Locate every cell, classifying each as a parasitized RBC, an uninfected RBC, or a WBC.
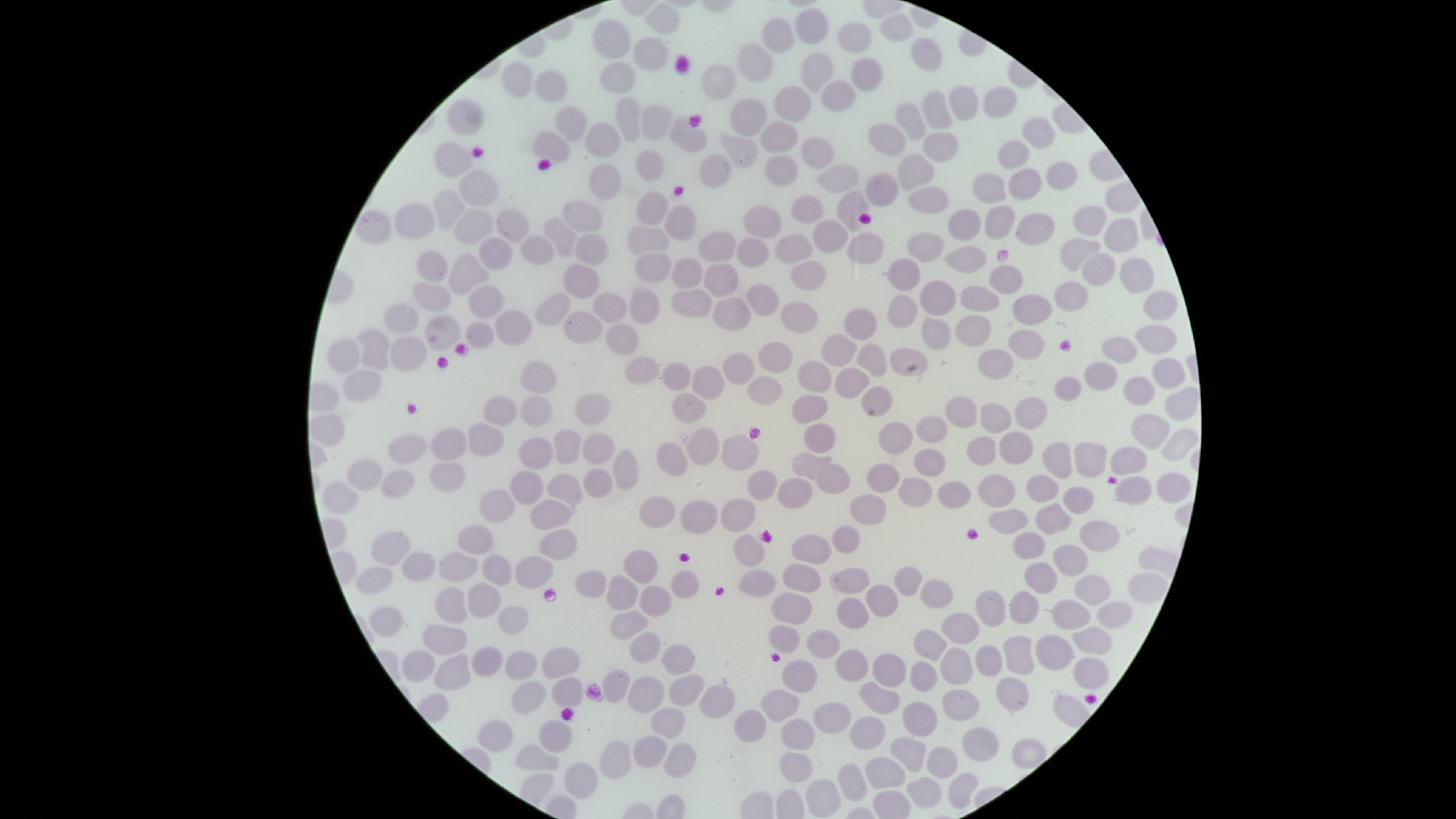
No parasitized RBCs identified.
Approximate bounding boxes as [left, top, right, bottom] in pixels.
Uninfected RBCs: [646, 4, 679, 34], [796, 9, 827, 43], [880, 15, 912, 41], [762, 17, 794, 53], [592, 20, 630, 60], [838, 24, 870, 53], [633, 37, 667, 72], [912, 37, 942, 71], [738, 43, 773, 81], [802, 52, 832, 90], [851, 58, 884, 92], [502, 62, 532, 98], [600, 62, 635, 93], [702, 64, 737, 100], [535, 72, 567, 101], [823, 82, 855, 114], [948, 84, 978, 121], [983, 85, 1017, 118], [774, 87, 810, 121], [922, 90, 953, 130], [616, 97, 639, 142], [729, 98, 766, 137], [449, 101, 483, 136], [895, 102, 925, 140], [643, 104, 671, 141], [556, 107, 588, 141], [1022, 117, 1055, 149], [670, 118, 707, 151], [586, 122, 621, 157], [761, 123, 798, 153], [869, 124, 906, 156], [534, 131, 569, 162], [719, 133, 758, 169], [924, 133, 957, 162], [801, 138, 834, 169], [997, 140, 1030, 169], [435, 142, 472, 177], [636, 150, 662, 181], [698, 153, 732, 188], [897, 154, 934, 189], [764, 156, 797, 185], [1046, 162, 1078, 190], [817, 163, 860, 194], [587, 164, 621, 201], [1008, 168, 1042, 200], [459, 170, 497, 206], [865, 173, 897, 206], [973, 173, 1006, 203], [909, 187, 949, 214], [837, 190, 870, 232], [433, 191, 465, 230], [637, 193, 667, 225], [792, 195, 822, 225], [563, 201, 602, 232], [395, 204, 435, 239], [665, 205, 695, 240], [742, 205, 783, 239], [984, 206, 1016, 240], [1074, 206, 1106, 235], [354, 209, 392, 243], [454, 210, 492, 243], [497, 210, 528, 242], [949, 210, 980, 241], [1016, 213, 1055, 245], [544, 216, 577, 258], [1105, 218, 1139, 252], [811, 221, 848, 253], [628, 226, 670, 254], [699, 231, 735, 264], [845, 232, 884, 264], [908, 233, 944, 262], [775, 234, 813, 265], [520, 235, 553, 265], [576, 235, 607, 266], [478, 237, 513, 270], [737, 237, 769, 268], [1060, 239, 1099, 271], [945, 246, 988, 273], [418, 250, 447, 282], [449, 252, 489, 296], [636, 253, 672, 282], [1082, 254, 1114, 286], [1120, 256, 1154, 293], [888, 258, 920, 291], [671, 259, 702, 289], [790, 260, 826, 290], [703, 263, 738, 297], [564, 264, 598, 298], [989, 264, 1023, 294], [919, 281, 955, 316], [1055, 282, 1088, 311], [412, 283, 451, 311], [747, 284, 778, 315], [469, 285, 503, 318], [960, 286, 999, 312], [671, 289, 712, 318], [630, 290, 660, 324], [1143, 290, 1178, 320], [593, 292, 627, 323], [536, 294, 570, 326], [888, 294, 917, 329], [1013, 294, 1052, 325], [714, 298, 751, 331], [781, 301, 818, 332], [383, 304, 419, 335], [843, 308, 877, 342], [496, 310, 533, 344], [564, 310, 602, 344], [426, 315, 460, 350], [956, 315, 991, 345], [920, 317, 951, 350], [466, 322, 494, 351], [607, 325, 639, 357], [1136, 326, 1176, 354], [357, 330, 389, 370], [1009, 331, 1044, 358], [821, 334, 857, 366], [391, 337, 426, 370], [1102, 338, 1136, 363], [328, 339, 360, 372], [758, 341, 793, 373], [856, 343, 887, 378], [890, 348, 928, 376], [978, 350, 1012, 378], [721, 353, 754, 385], [625, 356, 660, 385], [1153, 358, 1185, 390], [520, 360, 557, 394], [797, 361, 832, 391], [662, 363, 691, 391], [1084, 363, 1117, 391], [693, 366, 725, 400], [836, 367, 870, 398], [344, 370, 382, 402], [749, 376, 783, 404], [1122, 376, 1155, 406], [1056, 378, 1081, 402], [863, 385, 893, 416], [673, 393, 707, 423], [576, 394, 610, 426], [792, 395, 828, 423], [520, 396, 551, 426], [946, 396, 976, 428], [483, 397, 516, 426], [1015, 398, 1046, 429], [979, 403, 1011, 432], [1132, 413, 1170, 449], [917, 416, 947, 442], [879, 422, 913, 455], [468, 423, 504, 456], [804, 424, 836, 452], [688, 427, 719, 465], [1163, 427, 1198, 461], [433, 429, 467, 461], [554, 430, 581, 464], [1000, 432, 1034, 465], [583, 433, 615, 464], [723, 434, 758, 470], [389, 436, 425, 465], [967, 436, 996, 467], [519, 437, 554, 470], [1044, 441, 1072, 480], [657, 442, 689, 477], [1073, 442, 1106, 478], [613, 448, 638, 490], [914, 448, 944, 476], [1110, 448, 1146, 473], [793, 452, 831, 480], [348, 458, 384, 490], [430, 462, 466, 491], [815, 463, 850, 494], [867, 464, 899, 493], [584, 469, 613, 498], [748, 469, 775, 500], [381, 470, 416, 499], [511, 471, 544, 505], [547, 473, 583, 507], [1156, 473, 1190, 503], [978, 474, 1015, 508], [1026, 475, 1059, 502], [779, 477, 811, 509], [898, 477, 931, 507], [1115, 478, 1151, 506], [323, 482, 358, 514], [937, 482, 971, 509], [1063, 487, 1094, 514], [480, 489, 516, 523], [850, 494, 888, 526], [638, 496, 676, 527], [721, 497, 757, 532], [532, 498, 571, 530], [678, 499, 717, 535], [1034, 502, 1073, 534], [989, 509, 1029, 535], [1080, 520, 1121, 553], [457, 524, 493, 554], [833, 526, 861, 554], [541, 529, 577, 559], [371, 530, 411, 566], [1014, 532, 1045, 558], [734, 533, 766, 567], [791, 535, 833, 564], [1053, 544, 1087, 575], [624, 551, 657, 582], [439, 552, 478, 582], [401, 553, 435, 582], [483, 556, 511, 586], [516, 556, 553, 588], [1024, 562, 1057, 593], [784, 564, 822, 592], [354, 567, 393, 593], [832, 568, 870, 594], [893, 568, 923, 597], [739, 569, 777, 597], [671, 570, 699, 598], [1129, 573, 1165, 602], [607, 574, 638, 610], [1075, 575, 1111, 606], [919, 579, 954, 608], [468, 583, 502, 618], [864, 584, 899, 618], [640, 585, 673, 618], [434, 586, 467, 625], [976, 590, 1005, 627], [1010, 590, 1039, 624], [773, 591, 811, 624], [837, 597, 870, 629], [1052, 599, 1089, 630], [1097, 601, 1132, 628], [370, 606, 402, 636], [499, 607, 529, 634], [610, 611, 649, 640], [942, 611, 980, 644], [770, 624, 800, 651], [421, 625, 467, 654], [1072, 626, 1112, 654], [915, 629, 948, 660], [807, 630, 841, 659], [631, 633, 660, 661], [1034, 635, 1072, 670], [1003, 636, 1034, 673], [663, 643, 695, 675], [976, 645, 1003, 677], [473, 646, 502, 677], [941, 647, 973, 685], [542, 648, 581, 681], [835, 649, 868, 683], [401, 650, 434, 682], [506, 651, 538, 681], [872, 653, 906, 687], [434, 654, 470, 690], [1074, 657, 1108, 690], [782, 660, 818, 692], [910, 662, 936, 691], [604, 670, 629, 701], [669, 674, 703, 706], [628, 676, 663, 712], [553, 677, 584, 707], [996, 677, 1029, 711], [512, 682, 545, 713], [860, 684, 899, 714], [702, 685, 734, 718], [762, 687, 799, 722], [943, 690, 979, 720], [904, 702, 937, 736], [814, 703, 849, 733], [651, 708, 685, 737], [734, 710, 766, 743], [849, 716, 885, 750], [477, 719, 513, 753], [780, 719, 813, 751], [540, 720, 572, 751], [962, 727, 998, 761], [633, 736, 667, 769], [890, 737, 926, 773], [1012, 738, 1045, 768], [599, 740, 632, 778], [663, 743, 697, 778], [517, 744, 559, 771], [926, 747, 957, 779], [780, 752, 812, 782], [865, 757, 905, 790], [565, 763, 597, 797], [837, 763, 866, 802], [949, 771, 979, 809], [906, 777, 942, 807], [805, 780, 840, 815].
No WBCs identified.

capture = smartphone photograph through the microscope eyepiece
visible region = circular
stain = Giemsa
image size = 1456×819 pixels
field of view = single
preparation = thin smear of blood